State which parasite is depicted.
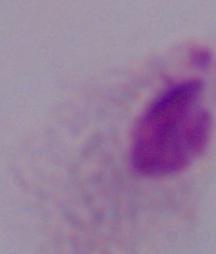

This is a trichomonad.

modality: micrograph
magnification: 1000x